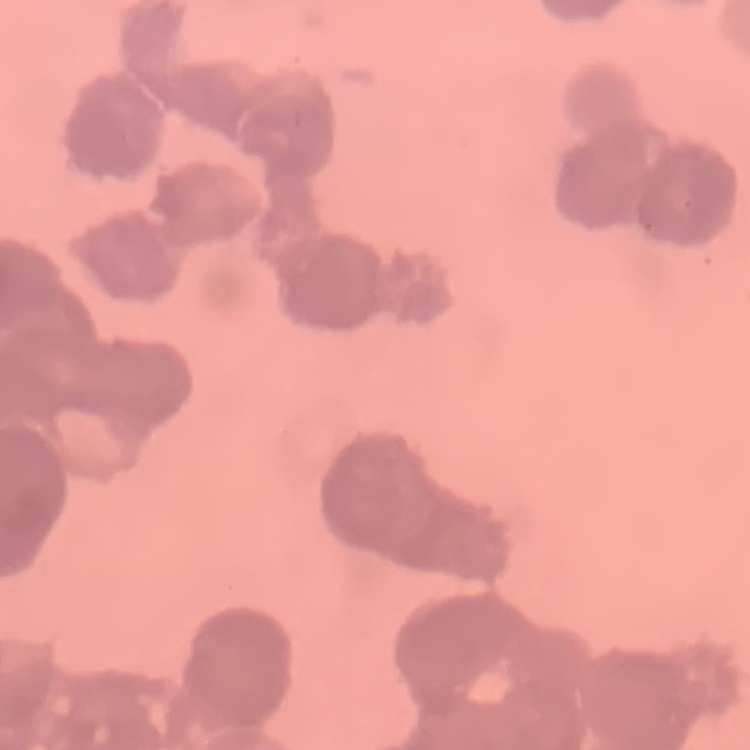
erythrocyte morphology = rouleaux formation
preparation = thin peripheral smear
image type = one tile cut from a larger photomicrograph
stain = Field's or Giemsa